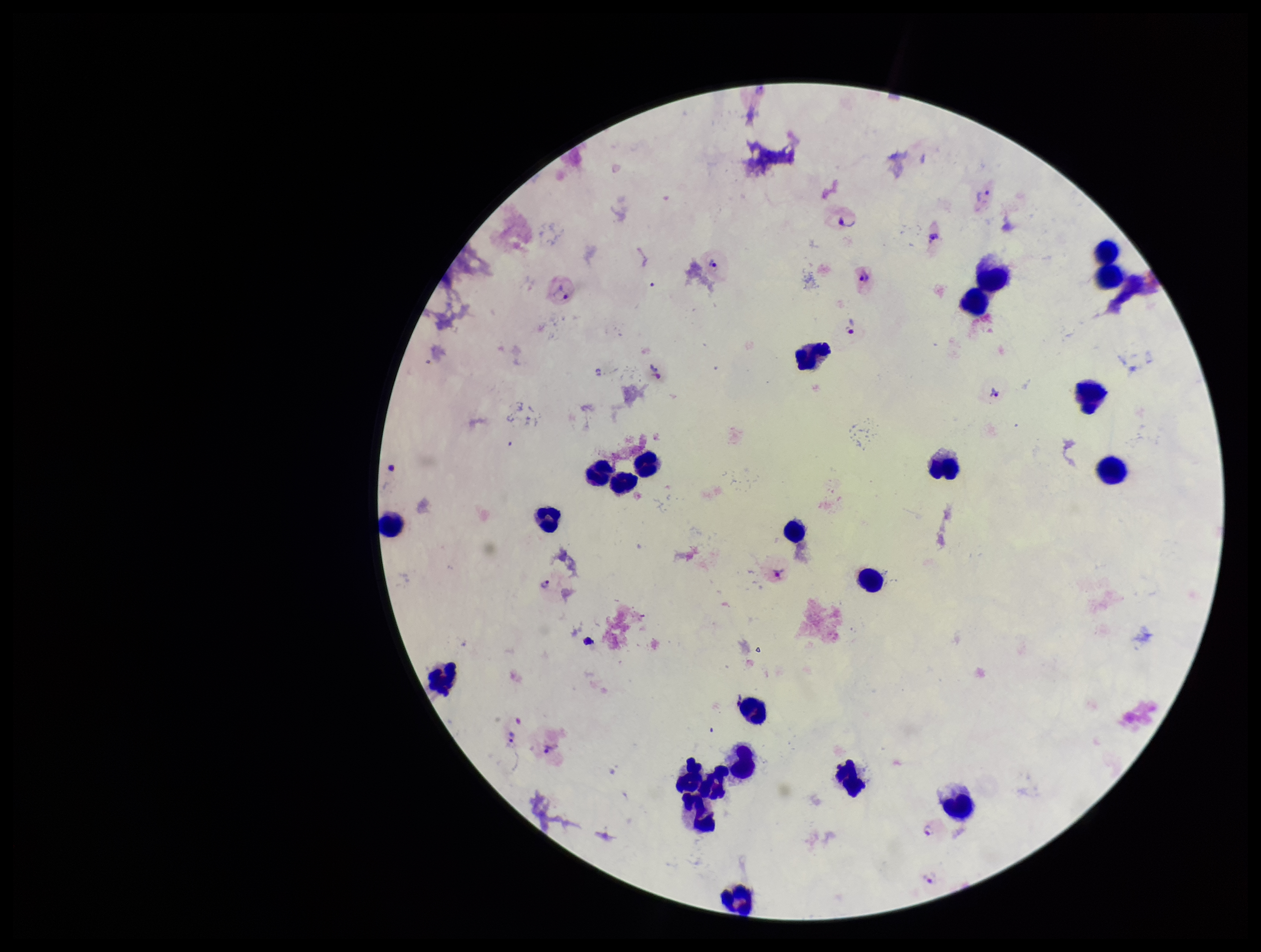
capture = smartphone photograph through the microscope eyepiece
stain = Giemsa
species reported for this patient = Plasmodium vivax
preparation = thick blood smear
field of view = single
patient malaria status = positive
parasite count = 12
image size = 1261×952 pixels
leukocyte count = 23
Plasmodium parasites = detected